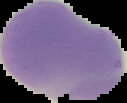
The area outside the segmented cell region is set to black. Image is 127×103 pixels. Malaria status: uninfected. From a thin blood smear.